Locate leukocytes (white blood cells).
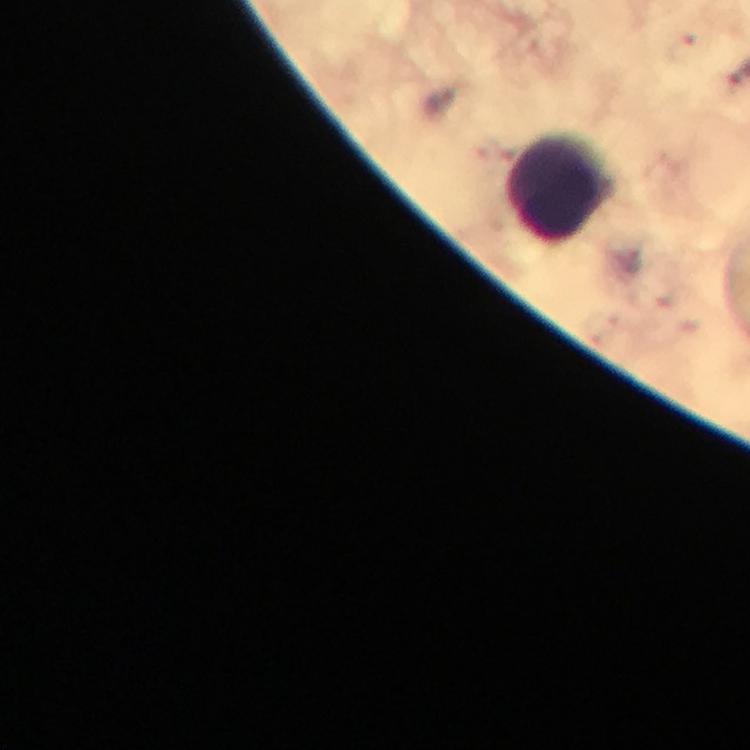
Approximate centers as (x, y) in pixels.
Leukocytes: (559, 187).

{
  "stain": "Giemsa",
  "magnification": "100x",
  "preparation": "thick smear",
  "plasmodium_parasites": "none seen",
  "immersion_oil": "used",
  "context": "from a diagnostic examination for malaria",
  "image_size": "750×750 pixels",
  "cropped_from": "one field of view",
  "capture": "smartphone photograph through a microscope"
}